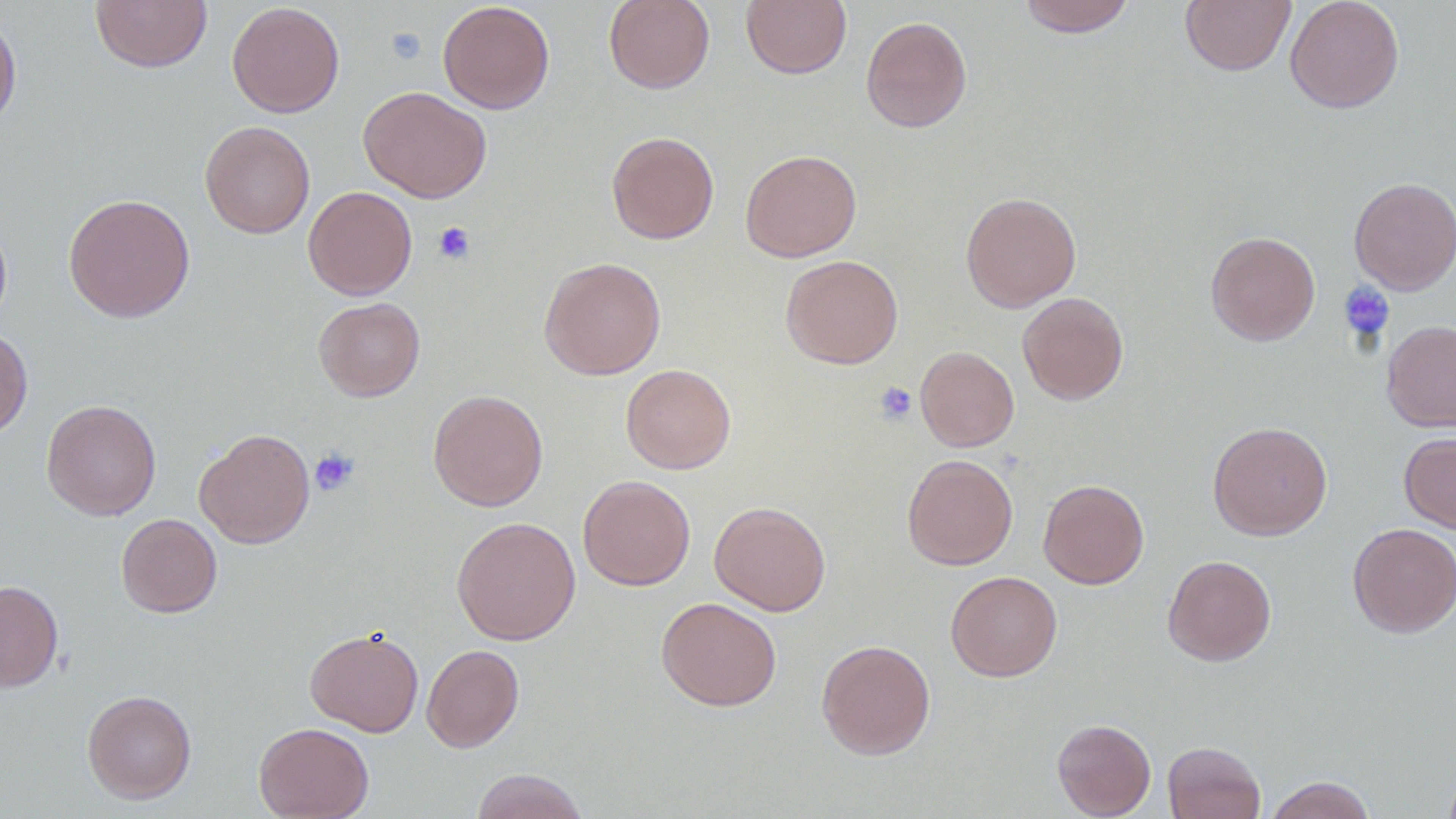

Approximate bounding boxes as [x1, y1, x2, y2] in pixels. Platelet locations: [386, 28, 426, 64], [433, 222, 475, 265], [1338, 281, 1395, 343], [874, 381, 917, 424], [310, 448, 359, 496]. Uninfected red blood cell locations: [89, 0, 213, 73], [603, 0, 714, 94], [741, 0, 852, 79], [1017, 0, 1137, 37], [1179, 0, 1296, 76], [1284, 0, 1404, 113], [438, 1, 555, 114], [228, 2, 345, 117], [0, 8, 22, 135], [860, 15, 972, 133], [359, 85, 491, 203], [199, 121, 315, 238], [606, 131, 719, 244], [740, 149, 862, 262], [1349, 177, 1456, 295], [303, 186, 418, 300], [960, 191, 1081, 312], [63, 192, 195, 323], [0, 214, 12, 332], [1205, 231, 1320, 346], [780, 254, 904, 369], [539, 256, 666, 380], [1017, 292, 1129, 405], [313, 297, 425, 401], [1381, 320, 1456, 432], [0, 327, 33, 439], [915, 346, 1019, 452], [620, 363, 736, 474], [427, 389, 548, 511], [41, 399, 162, 520], [1208, 421, 1333, 540], [193, 428, 315, 549], [1399, 431, 1456, 534], [901, 453, 1018, 570], [578, 474, 696, 590], [1038, 478, 1149, 589], [709, 501, 831, 616], [116, 513, 222, 618], [451, 516, 581, 645], [1347, 522, 1456, 637], [1162, 554, 1277, 666], [945, 570, 1062, 682], [0, 580, 63, 692], [656, 596, 782, 711], [304, 627, 423, 737], [816, 639, 936, 760], [421, 644, 524, 752], [82, 689, 197, 804], [1052, 718, 1156, 818], [254, 722, 374, 819], [1162, 741, 1266, 819], [1442, 765, 1456, 819], [471, 768, 590, 819], [1263, 775, 1378, 819]. Slide-level diagnosis: negative for blood parasites. Image is 1456×819 pixels. Light microscopy. Thin blood film. Captured at 1000x magnification. Single field of view.